Assess the morphology of the red blood cells.
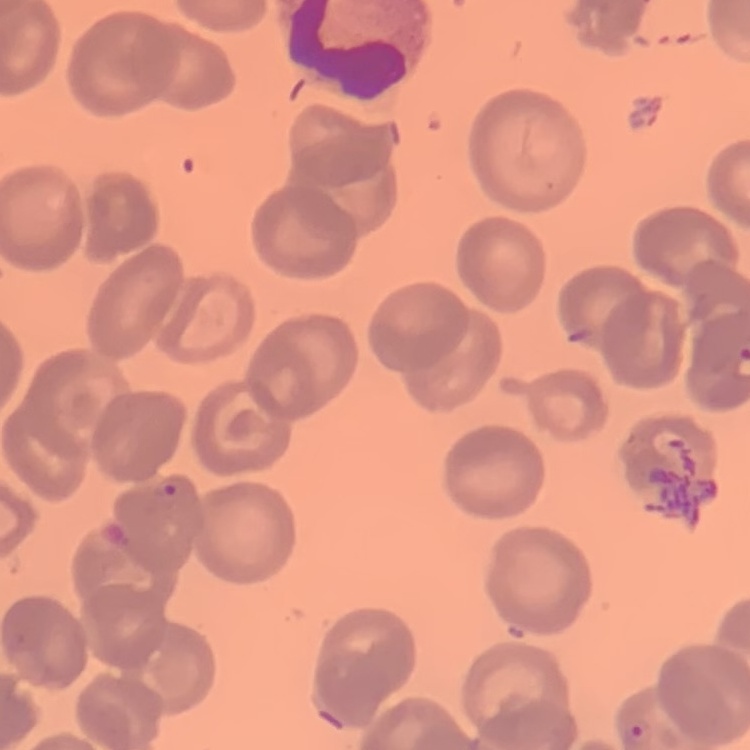

They show no rouleaux formation.

Stained with either Field's or Giemsa. One tile cut from a larger photomicrograph. Thin blood smear.